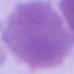

modality = micrograph
identification = erythrocyte
magnification = 1000x